Give the extent of all Plasmodium vivax-infected red blood cells.
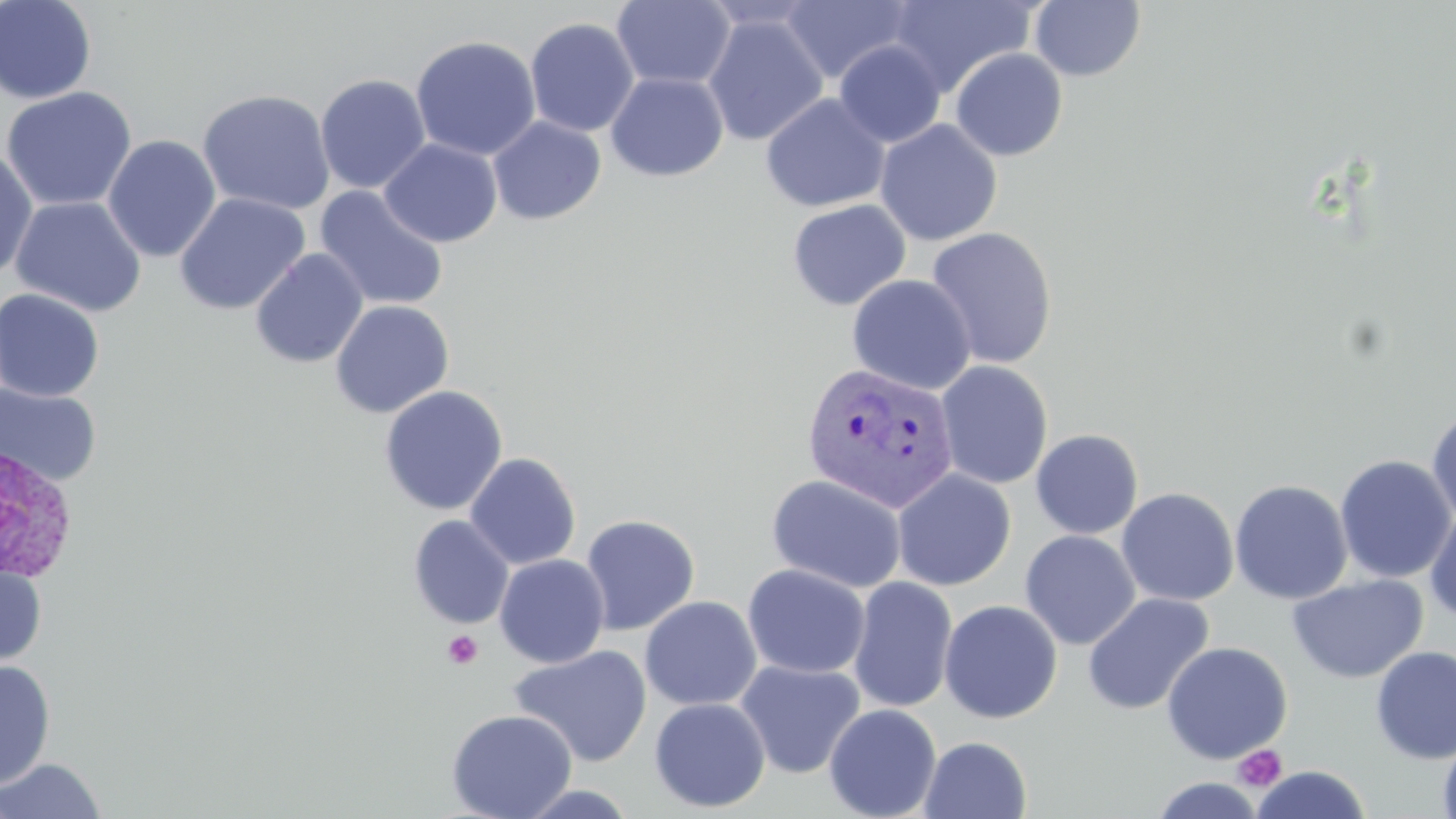
Approximate bounding boxes as (x1, y1, x2, y2) in pixels.
Plasmodium vivax-infected red blood cells: (801, 362, 960, 513), (0, 443, 79, 585).

Summary:
  - Platelet locations: (442, 630, 484, 670), (1232, 744, 1287, 792)
  - Uninfected red blood cell locations: (0, 0, 97, 104), (612, 0, 736, 91), (780, 0, 915, 85), (888, 0, 1036, 98), (699, 1, 824, 32), (1030, 1, 1146, 82), (702, 14, 828, 146), (524, 17, 639, 137), (410, 35, 541, 161), (833, 41, 946, 148), (949, 47, 1068, 162), (605, 72, 729, 182), (315, 73, 431, 194), (1, 86, 138, 212), (197, 88, 336, 216), (760, 93, 890, 212), (487, 115, 606, 225), (874, 119, 1003, 246), (102, 134, 221, 263), (380, 139, 502, 247), (0, 147, 39, 282), (314, 186, 449, 311), (174, 192, 310, 316), (10, 195, 147, 317), (786, 199, 911, 311), (924, 226, 1059, 370), (250, 248, 369, 368), (846, 274, 976, 395), (0, 288, 105, 402), (330, 299, 455, 419), (935, 360, 1053, 489), (0, 381, 102, 487), (379, 385, 508, 515), (1426, 404, 1456, 528), (1030, 429, 1144, 539), (464, 452, 581, 570), (1335, 454, 1455, 583), (892, 469, 1016, 591), (766, 473, 908, 594), (1229, 478, 1353, 604), (1116, 487, 1239, 607), (1424, 505, 1456, 626), (580, 513, 701, 635), (408, 515, 514, 629), (1019, 530, 1140, 650), (494, 554, 610, 668), (0, 558, 47, 669), (742, 563, 871, 679), (1287, 573, 1428, 683), (848, 576, 958, 713), (1082, 592, 1215, 716), (640, 596, 762, 710), (939, 599, 1063, 724), (1161, 641, 1293, 764), (508, 644, 653, 767), (1370, 646, 1456, 764), (0, 659, 56, 789), (735, 659, 866, 779), (649, 697, 771, 813), (824, 703, 942, 819), (446, 708, 577, 819), (1437, 733, 1456, 819), (920, 736, 1032, 819), (0, 757, 107, 818), (1250, 766, 1372, 818), (1147, 776, 1266, 818), (514, 782, 641, 817)
  - Slide-level diagnosis: Plasmodium vivax
  - Modality: light microscopy
  - Image size: 1456×819 pixels
  - Preparation: thin blood film
  - Field of view: single
  - Stain: May-Grünwald-Giemsa
  - Magnification: 1000x